Describe the morphology of the red blood cells.
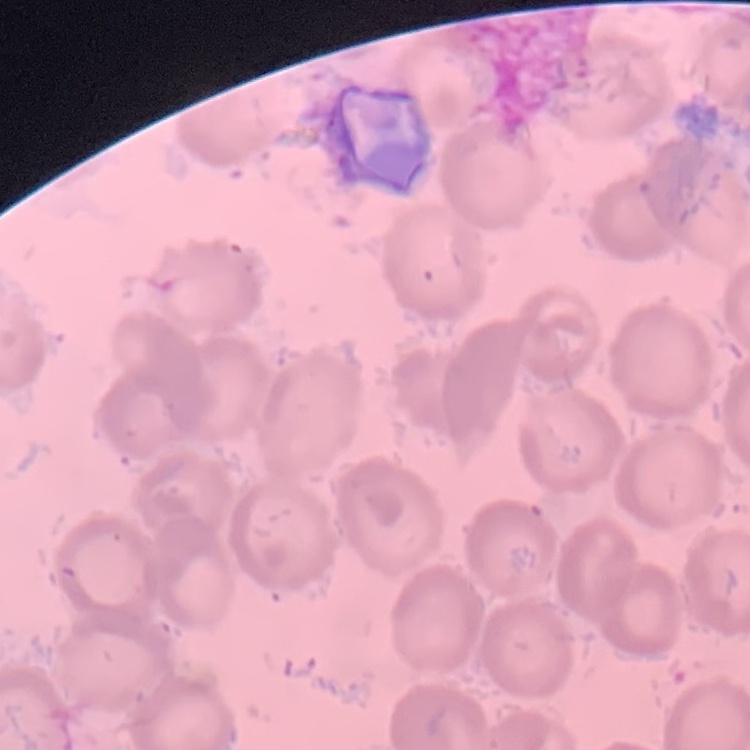
They show no rouleaux formation.

stain = Field's or Giemsa
preparation = thin blood smear
image type = square crop of a larger photomicrograph